Report the malaria status of this cell.
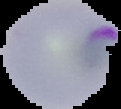

It is parasitized.

image size = 121×109 pixels
image type = segmented cell region on a black background
preparation = thin blood film